Name the blood parasite species.
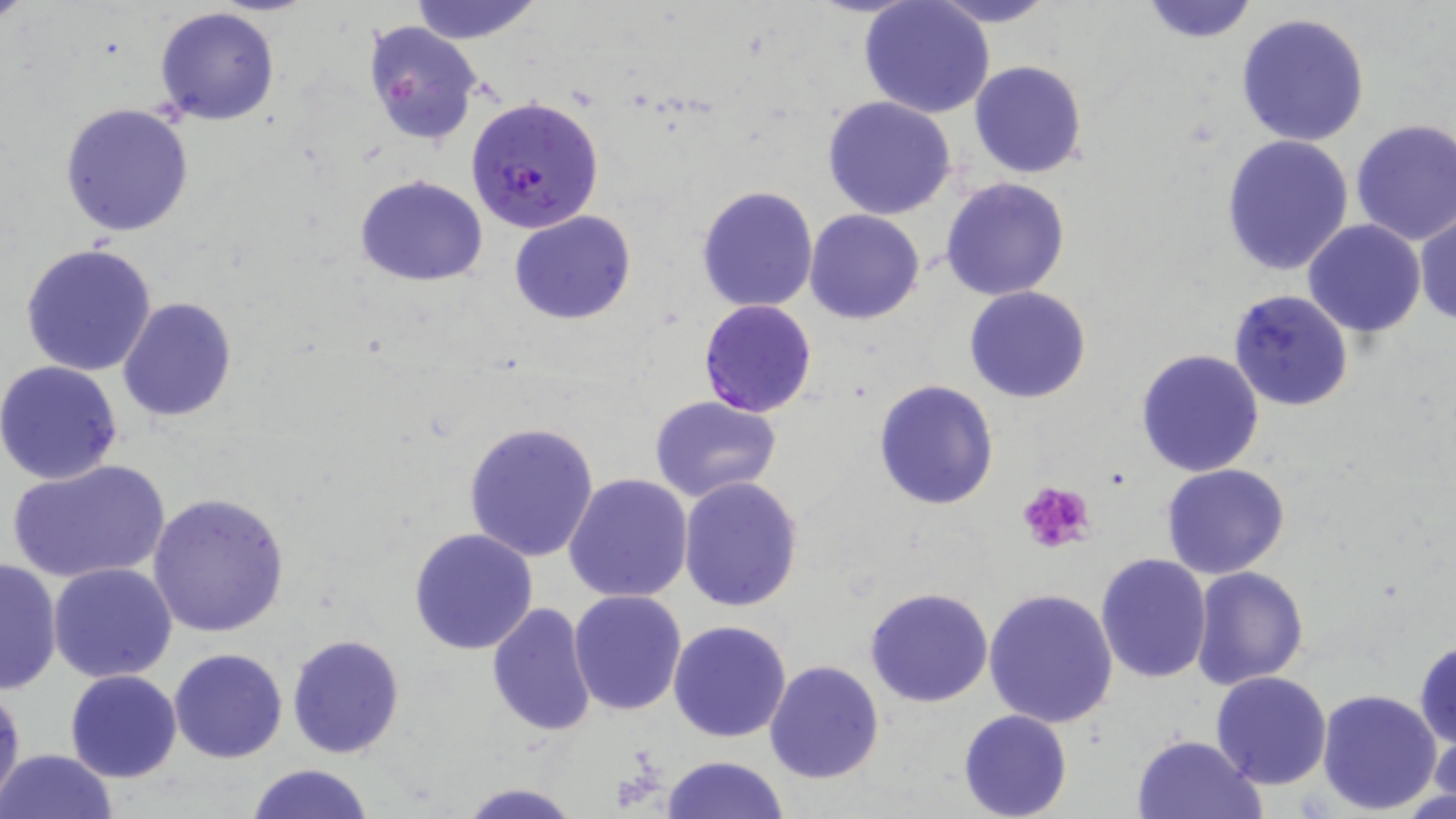

Plasmodium falciparum.

Approximate bounding boxes as (x1, y1, x2, y2) in pixels. Uninfected red blood cell locations: (0, 0, 36, 28), (408, 0, 543, 44), (860, 0, 995, 120), (927, 0, 1060, 26), (1138, 0, 1260, 43), (153, 6, 280, 126), (1235, 11, 1370, 146), (362, 20, 484, 147), (969, 60, 1089, 180), (822, 95, 957, 219), (60, 102, 194, 236), (1349, 119, 1456, 247), (1220, 134, 1355, 275), (354, 175, 488, 286), (941, 176, 1071, 301), (697, 186, 819, 312), (510, 210, 636, 325), (806, 210, 925, 325), (1413, 211, 1456, 328), (1302, 219, 1427, 337), (22, 242, 158, 377), (963, 285, 1092, 403), (1228, 289, 1354, 413), (117, 298, 237, 422), (1135, 348, 1265, 478), (0, 360, 125, 486), (872, 380, 1000, 510), (650, 396, 781, 503), (465, 420, 600, 561), (6, 458, 170, 585), (1161, 463, 1290, 580), (563, 474, 694, 605), (678, 476, 804, 612), (148, 492, 292, 636), (408, 527, 538, 655), (1095, 553, 1213, 684), (1, 555, 63, 694), (48, 562, 178, 683), (1190, 565, 1309, 690), (865, 586, 994, 708), (983, 587, 1119, 728), (568, 589, 688, 717), (485, 601, 596, 738), (667, 619, 793, 742), (286, 633, 408, 758), (1414, 639, 1456, 749), (169, 648, 289, 763), (765, 661, 884, 784), (65, 670, 181, 783), (1209, 671, 1332, 790), (0, 680, 24, 813), (1315, 688, 1442, 815), (958, 710, 1072, 819), (1428, 731, 1455, 811), (1129, 732, 1267, 818), (1, 748, 118, 819), (659, 755, 789, 819), (244, 763, 375, 819), (458, 782, 581, 818). Platelet locations: (1017, 478, 1098, 554). Plasmodium falciparum-infected red blood cell locations: (466, 97, 605, 234), (698, 299, 819, 419). Image is 1456×819 pixels. 1000x magnification. Light microscopy. May-Grünwald-Giemsa stain. Thin blood smear. Single field of view.